Describe the morphology of the red blood cells.
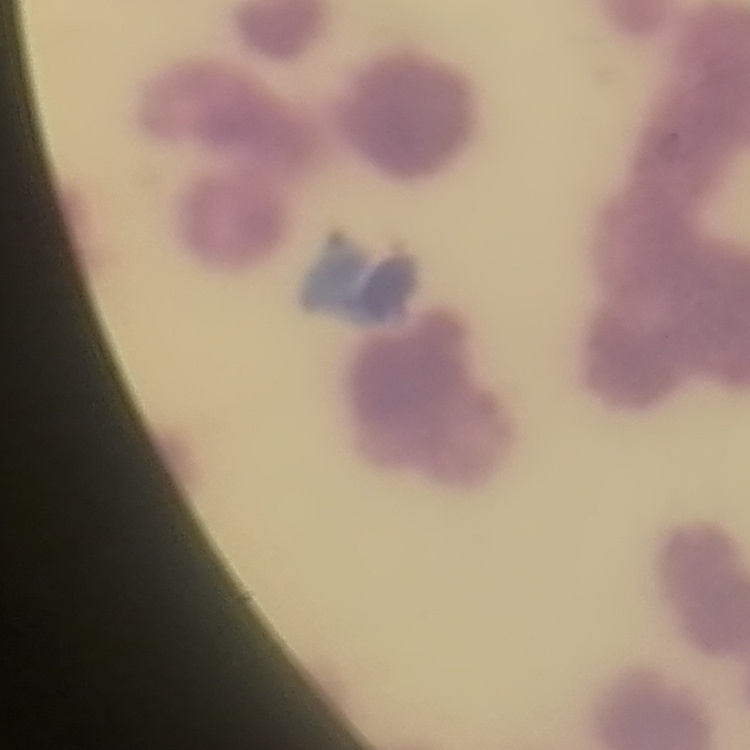
Rouleaux formation.

image type = square crop of a larger photomicrograph
preparation = thin blood smear
stain = Field's or Giemsa